Outline each white blood cell.
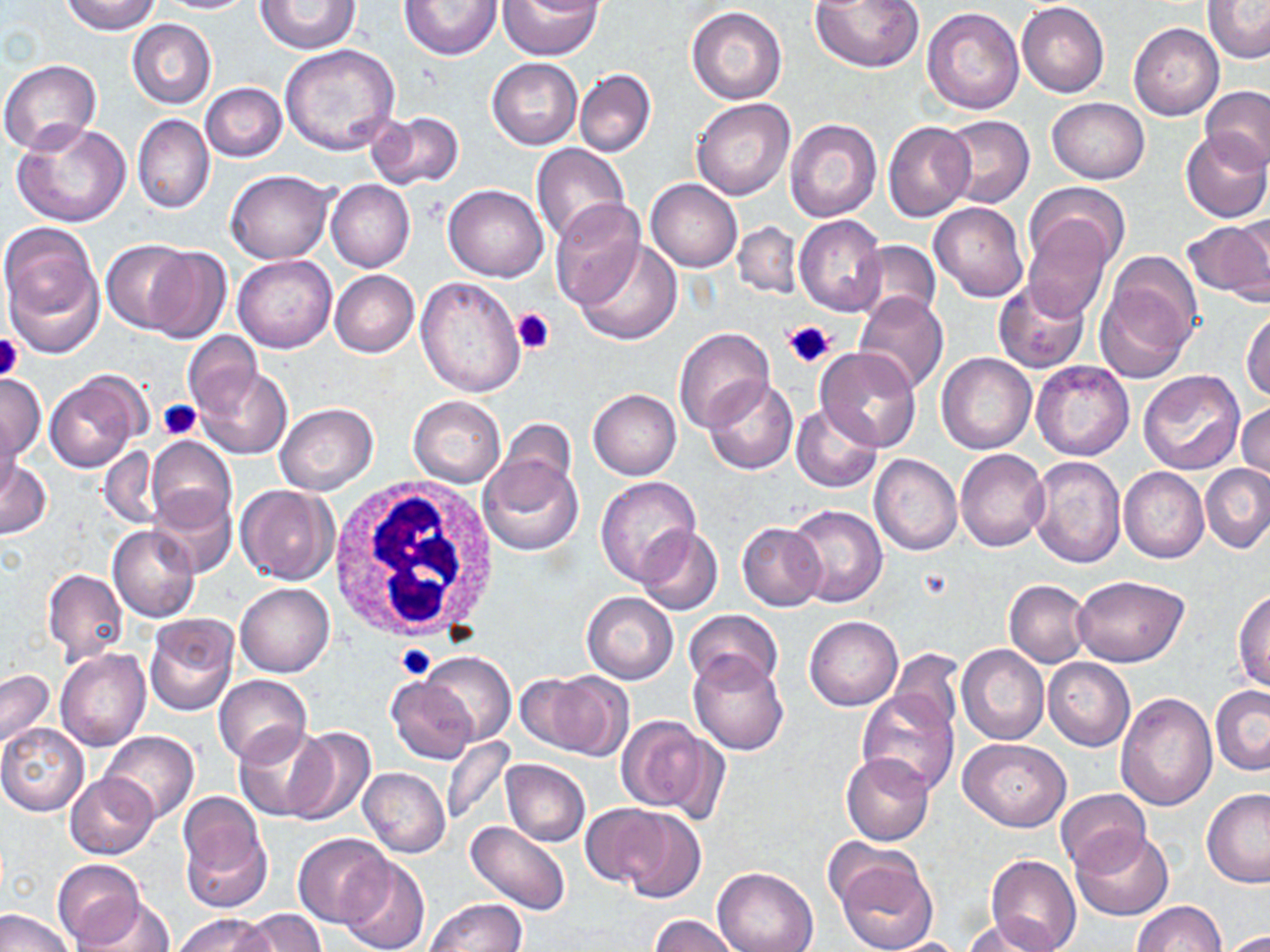
Approximate bounding boxes as named x1/y1/x2/y2 corners in pixels.
White blood cells: (x1=328, y1=477, x2=500, y2=645).

{
  "slide_level_diagnosis": "no evidence of blood parasites",
  "uninfected_red_blood_cell_locations": "approximate bounding boxes as named x1/y1/x2/y2 corners in pixels: (x1=62, y1=0, x2=161, y2=36), (x1=155, y1=0, x2=255, y2=14), (x1=255, y1=0, x2=360, y2=53), (x1=399, y1=0, x2=502, y2=60), (x1=496, y1=0, x2=602, y2=59), (x1=809, y1=0, x2=925, y2=72), (x1=1017, y1=1, x2=1109, y2=98), (x1=1201, y1=1, x2=1270, y2=65), (x1=686, y1=6, x2=787, y2=104), (x1=922, y1=7, x2=1025, y2=113), (x1=127, y1=19, x2=216, y2=108), (x1=1129, y1=23, x2=1224, y2=121), (x1=280, y1=44, x2=400, y2=155), (x1=487, y1=57, x2=582, y2=150), (x1=0, y1=59, x2=103, y2=156), (x1=574, y1=69, x2=656, y2=158), (x1=200, y1=82, x2=287, y2=163), (x1=1201, y1=85, x2=1270, y2=171), (x1=1047, y1=97, x2=1148, y2=184), (x1=692, y1=99, x2=794, y2=200), (x1=367, y1=111, x2=466, y2=191), (x1=132, y1=114, x2=214, y2=213), (x1=940, y1=115, x2=1034, y2=209), (x1=784, y1=118, x2=882, y2=221), (x1=12, y1=120, x2=131, y2=227), (x1=883, y1=120, x2=975, y2=221), (x1=1181, y1=131, x2=1270, y2=224), (x1=531, y1=143, x2=630, y2=243), (x1=226, y1=170, x2=332, y2=264), (x1=645, y1=179, x2=742, y2=272), (x1=327, y1=180, x2=414, y2=272), (x1=1026, y1=181, x2=1130, y2=273), (x1=443, y1=184, x2=550, y2=282), (x1=928, y1=201, x2=1028, y2=301), (x1=550, y1=204, x2=645, y2=310), (x1=795, y1=214, x2=887, y2=317), (x1=1230, y1=216, x2=1270, y2=302), (x1=1184, y1=217, x2=1270, y2=304), (x1=1021, y1=218, x2=1113, y2=320), (x1=732, y1=220, x2=804, y2=299), (x1=1, y1=222, x2=103, y2=353), (x1=573, y1=239, x2=684, y2=346), (x1=101, y1=240, x2=196, y2=334), (x1=852, y1=240, x2=941, y2=327), (x1=143, y1=246, x2=233, y2=343), (x1=233, y1=254, x2=337, y2=353), (x1=1094, y1=260, x2=1198, y2=382), (x1=329, y1=270, x2=420, y2=358), (x1=416, y1=276, x2=526, y2=399), (x1=994, y1=279, x2=1090, y2=373), (x1=853, y1=290, x2=948, y2=396), (x1=1241, y1=306, x2=1270, y2=402), (x1=673, y1=327, x2=776, y2=432), (x1=183, y1=332, x2=264, y2=418), (x1=815, y1=348, x2=923, y2=452), (x1=937, y1=353, x2=1037, y2=454), (x1=1031, y1=360, x2=1135, y2=460), (x1=194, y1=366, x2=292, y2=459), (x1=1138, y1=369, x2=1247, y2=475), (x1=44, y1=371, x2=144, y2=474), (x1=0, y1=375, x2=45, y2=462), (x1=704, y1=376, x2=798, y2=474), (x1=588, y1=389, x2=681, y2=479), (x1=408, y1=397, x2=506, y2=486), (x1=274, y1=402, x2=378, y2=495), (x1=791, y1=403, x2=882, y2=494), (x1=1237, y1=403, x2=1270, y2=486), (x1=0, y1=411, x2=21, y2=503), (x1=492, y1=420, x2=579, y2=501), (x1=148, y1=436, x2=237, y2=533), (x1=99, y1=446, x2=165, y2=531), (x1=956, y1=449, x2=1050, y2=552), (x1=869, y1=453, x2=962, y2=556), (x1=478, y1=455, x2=583, y2=556), (x1=1025, y1=455, x2=1126, y2=569), (x1=0, y1=460, x2=51, y2=539), (x1=1202, y1=465, x2=1270, y2=555), (x1=1118, y1=467, x2=1209, y2=563), (x1=594, y1=477, x2=701, y2=586), (x1=235, y1=485, x2=339, y2=585), (x1=149, y1=490, x2=238, y2=577), (x1=785, y1=503, x2=889, y2=608), (x1=737, y1=522, x2=828, y2=612), (x1=108, y1=525, x2=201, y2=624), (x1=635, y1=525, x2=723, y2=616), (x1=42, y1=569, x2=128, y2=665), (x1=1073, y1=575, x2=1189, y2=667), (x1=1004, y1=579, x2=1092, y2=668), (x1=234, y1=583, x2=333, y2=677), (x1=1233, y1=588, x2=1270, y2=692), (x1=582, y1=591, x2=678, y2=684), (x1=682, y1=608, x2=783, y2=693), (x1=143, y1=614, x2=239, y2=716), (x1=804, y1=615, x2=903, y2=710), (x1=957, y1=644, x2=1049, y2=745), (x1=888, y1=648, x2=964, y2=735), (x1=55, y1=649, x2=151, y2=752), (x1=419, y1=651, x2=517, y2=746), (x1=687, y1=652, x2=790, y2=755), (x1=1042, y1=657, x2=1135, y2=750), (x1=1, y1=669, x2=54, y2=749), (x1=523, y1=670, x2=632, y2=761), (x1=213, y1=674, x2=312, y2=765), (x1=387, y1=676, x2=479, y2=765), (x1=1210, y1=686, x2=1270, y2=775), (x1=857, y1=691, x2=960, y2=795), (x1=1115, y1=693, x2=1217, y2=811), (x1=615, y1=716, x2=721, y2=818), (x1=0, y1=723, x2=89, y2=815), (x1=232, y1=724, x2=332, y2=821), (x1=281, y1=726, x2=375, y2=827), (x1=101, y1=731, x2=199, y2=824), (x1=441, y1=737, x2=515, y2=827), (x1=959, y1=738, x2=1070, y2=830), (x1=841, y1=752, x2=935, y2=846), (x1=501, y1=758, x2=590, y2=847), (x1=358, y1=767, x2=450, y2=858), (x1=66, y1=773, x2=160, y2=860), (x1=1201, y1=787, x2=1270, y2=887), (x1=1054, y1=788, x2=1151, y2=873), (x1=177, y1=790, x2=271, y2=911), (x1=580, y1=804, x2=676, y2=891), (x1=611, y1=807, x2=707, y2=904), (x1=465, y1=820, x2=571, y2=916), (x1=1070, y1=827, x2=1173, y2=921), (x1=293, y1=832, x2=395, y2=928), (x1=829, y1=848, x2=938, y2=952), (x1=986, y1=854, x2=1081, y2=952), (x1=338, y1=856, x2=430, y2=952), (x1=52, y1=859, x2=146, y2=947), (x1=713, y1=867, x2=819, y2=952), (x1=73, y1=897, x2=174, y2=952), (x1=426, y1=898, x2=526, y2=950), (x1=1132, y1=902, x2=1227, y2=952), (x1=0, y1=909, x2=75, y2=952), (x1=237, y1=909, x2=327, y2=952), (x1=175, y1=914, x2=273, y2=952), (x1=963, y1=915, x2=1061, y2=951), (x1=650, y1=916, x2=740, y2=952), (x1=1220, y1=929, x2=1270, y2=951), (x1=880, y1=937, x2=974, y2=952)",
  "image_size": "1270×952 pixels",
  "platelet_locations": "approximate bounding boxes as named x1/y1/x2/y2 corners in pixels: (x1=512, y1=307, x2=556, y2=353), (x1=783, y1=319, x2=835, y2=370), (x1=0, y1=334, x2=24, y2=382), (x1=159, y1=398, x2=201, y2=440), (x1=397, y1=643, x2=437, y2=681)",
  "stain": "May-Grünwald-Giemsa",
  "magnification": "1000x",
  "modality": "optical microscopy",
  "field_of_view": "single",
  "preparation": "thin blood film"
}